State which cell type is depicted.
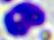
This is a leukocyte.

modality: photomicrograph
magnification: 400x